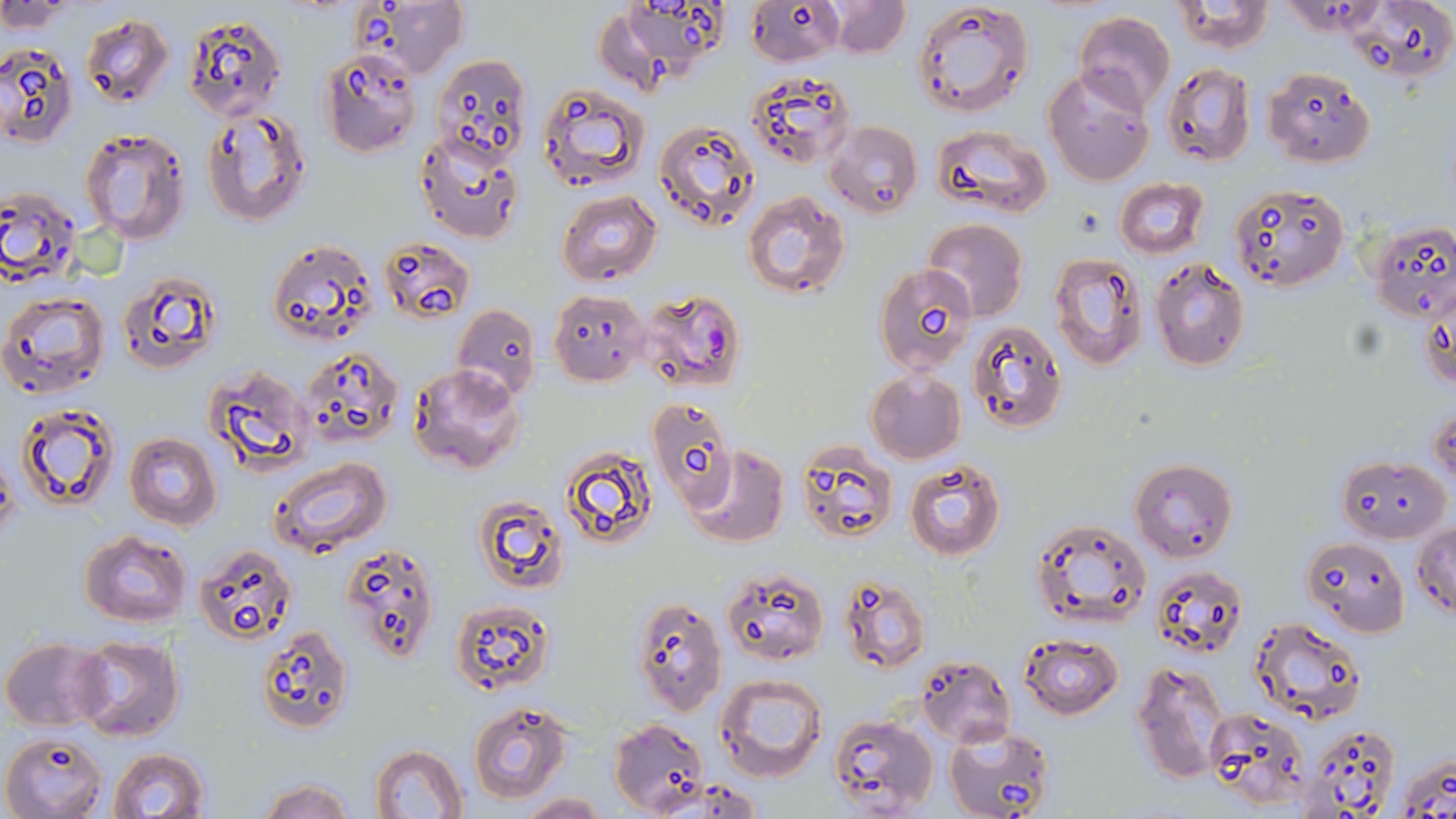

Approximate bounding boxes as [x1, y1, x2, y2] in pixels. Plasmodium falciparum-infected red blood cell locations: [640, 290, 744, 394]. Uninfected red blood cell locations: [827, 0, 911, 58], [0, 1, 72, 31], [358, 1, 469, 80], [616, 1, 728, 76], [910, 1, 1035, 117], [1172, 1, 1273, 55], [749, 3, 842, 65], [1075, 11, 1176, 113], [80, 13, 173, 108], [184, 14, 286, 122], [0, 42, 77, 150], [318, 48, 423, 157], [431, 54, 533, 170], [1162, 64, 1256, 166], [1042, 67, 1154, 186], [747, 68, 855, 169], [1263, 68, 1375, 167], [538, 83, 649, 191], [201, 109, 311, 226], [825, 120, 923, 219], [655, 121, 760, 230], [931, 123, 1053, 218], [79, 127, 190, 243], [415, 131, 524, 243], [1114, 178, 1209, 258], [1230, 181, 1348, 293], [0, 185, 82, 284], [557, 190, 661, 285], [743, 191, 850, 298], [1368, 218, 1456, 323], [923, 219, 1029, 320], [378, 236, 476, 324], [265, 237, 377, 347], [1049, 253, 1147, 369], [1149, 257, 1251, 372], [874, 262, 977, 375], [118, 271, 223, 374], [1419, 284, 1455, 400], [549, 289, 649, 386], [1, 290, 110, 400], [453, 304, 541, 400], [967, 320, 1066, 435], [298, 346, 403, 451], [407, 362, 524, 475], [205, 364, 311, 476], [864, 369, 965, 463], [650, 398, 746, 515], [16, 400, 119, 512], [1429, 404, 1456, 492], [124, 431, 222, 530], [558, 444, 660, 554], [795, 444, 898, 544], [686, 446, 788, 548], [1336, 454, 1449, 543], [269, 458, 390, 560], [904, 458, 1006, 560], [1131, 459, 1238, 565], [473, 496, 568, 595], [1028, 516, 1154, 629], [1411, 521, 1456, 618], [80, 530, 193, 627], [1301, 538, 1408, 637], [339, 541, 441, 664], [193, 543, 300, 647], [1151, 564, 1250, 659], [721, 567, 828, 666], [839, 577, 932, 674], [631, 595, 727, 716], [449, 599, 554, 694], [1249, 617, 1366, 727], [256, 625, 355, 734], [1018, 633, 1125, 719], [1, 636, 107, 731], [73, 636, 185, 741], [917, 654, 1016, 744], [1132, 659, 1229, 784], [715, 673, 830, 782], [468, 700, 571, 802], [1205, 708, 1310, 808], [826, 711, 937, 816], [609, 718, 709, 817], [944, 725, 1056, 819], [1301, 725, 1403, 817], [2, 731, 107, 818], [369, 744, 469, 819], [108, 747, 210, 819], [1395, 750, 1456, 819], [257, 778, 358, 819], [516, 793, 609, 818]. Slide-level diagnosis: Plasmodium falciparum. Image is 1456×819 pixels. Thin blood smear. One field of a larger specimen. 1000x magnification. Optical microscopy. May-Grünwald-Giemsa-stained preparation.